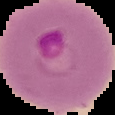
The area outside the segmented cell region is set to black. From a thin blood film. Image is 115×115 pixels. Result: malaria parasites identified.